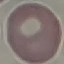

Summary:
  - Malaria status: uninfected
  - Capture: smartphone through the microscope eyepiece
  - Image type: automatically extracted cell patch, resized to 64 × 64 pixels
  - Stain: Giemsa
  - Preparation: thin blood film